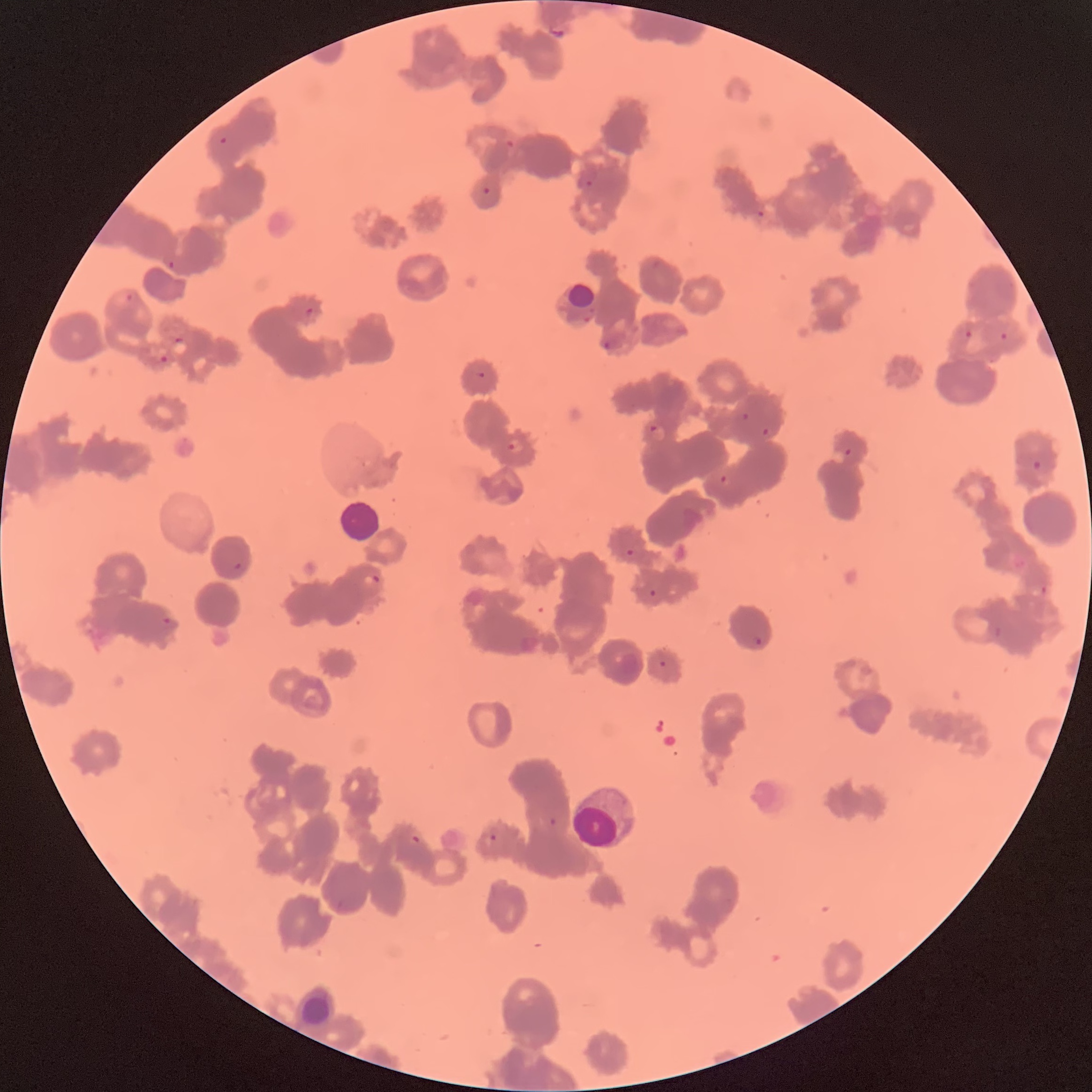

coordinate format = approximate bounding boxes as [x1, y1, x2, y2] in pixels
Plasmodium parasite locations = [548, 26, 567, 42], [219, 136, 227, 145], [504, 139, 516, 150], [584, 179, 593, 188], [483, 187, 491, 196], [756, 209, 767, 219], [167, 261, 175, 271], [125, 293, 133, 302], [305, 306, 314, 315], [965, 329, 974, 339], [999, 331, 1009, 341], [171, 336, 189, 355], [603, 340, 611, 351], [159, 354, 169, 364], [476, 371, 486, 378], [741, 412, 750, 421], [646, 422, 667, 443], [761, 427, 769, 437], [507, 443, 516, 450], [1031, 459, 1043, 472], [718, 473, 730, 485], [626, 548, 635, 558], [233, 560, 243, 572], [361, 573, 381, 587], [1040, 583, 1050, 595], [648, 588, 657, 597], [161, 617, 173, 627], [751, 635, 762, 647], [659, 660, 666, 668], [549, 816, 556, 826], [412, 833, 423, 845], [489, 833, 499, 843]
white blood cell locations = [339, 500, 381, 544]
Plasmodium parasites too small for a box (approximate centers as [x, y] in pixels) = [848, 451]
preparation = thin blood smear
modality = optical microscopy
red blood cell morphology = rouleaux formation
image size = 1092×1092 pixels